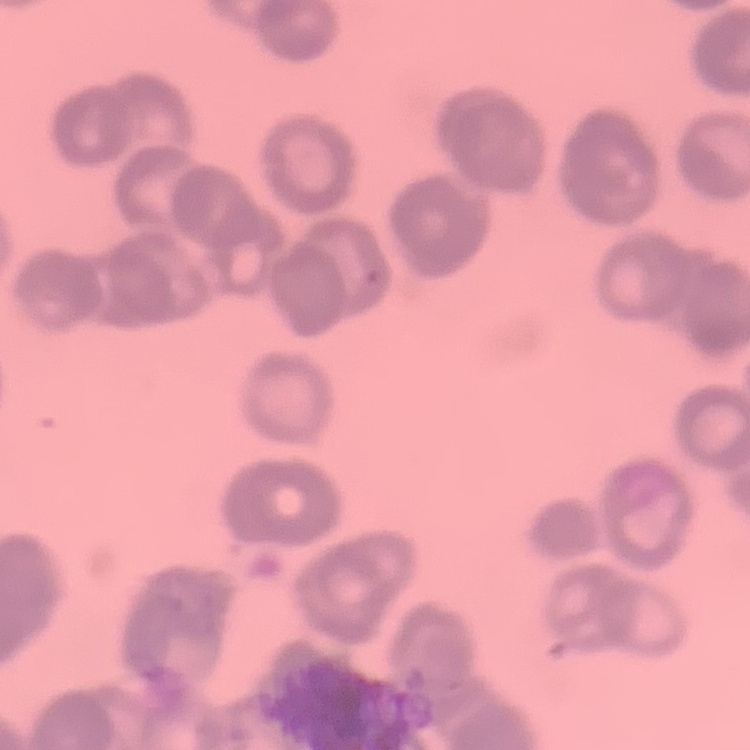
The red blood cells exhibit rouleaux formation. Thin peripheral smear. Field's or Giemsa stain. Square crop of a larger photomicrograph.